Assess the morphology of the red blood cells.
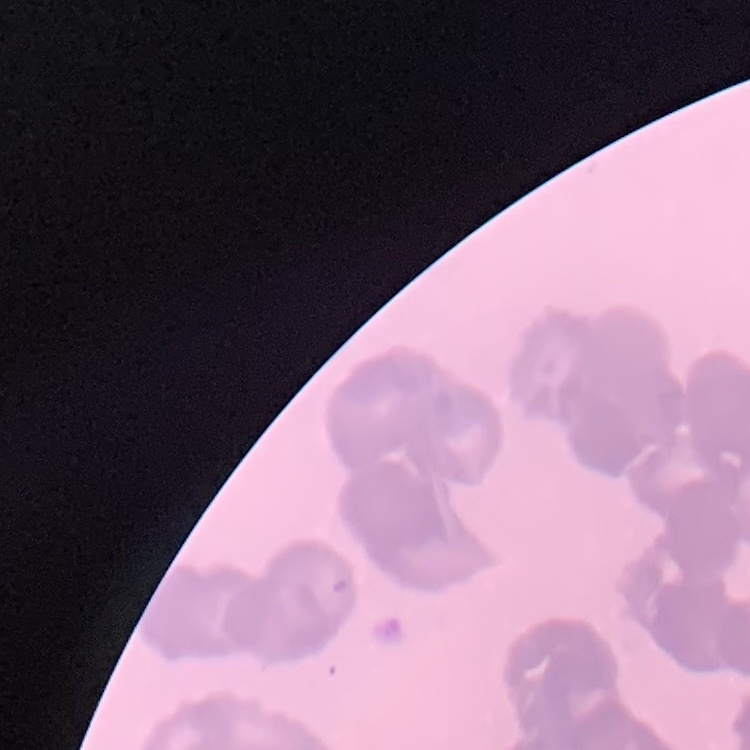

Rouleaux formation.

Thin blood smear. Field's or Giemsa stain. Square crop of a larger photomicrograph.